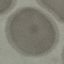
Result: no malaria parasites detected. Photographed with a smartphone camera at the microscope eyepiece. Cell patch, automatically extracted from a larger field of view and resized to 64 × 64 pixels. Giemsa stain. Thin blood smear.